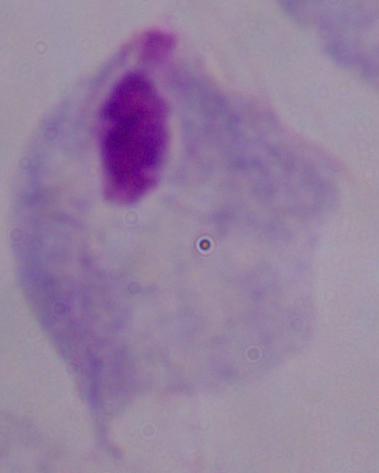
magnification: 1000x
identification: trichomonad
modality: photomicrograph